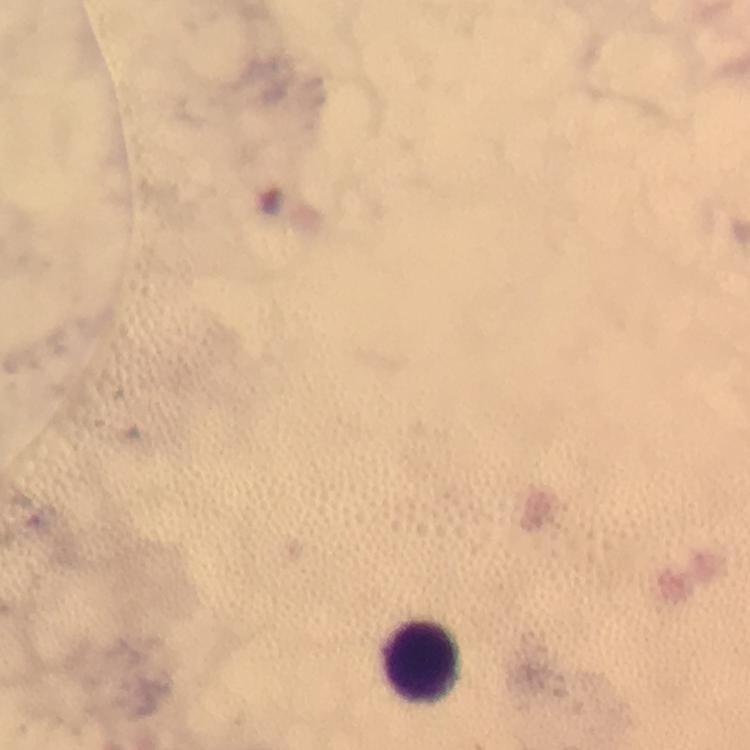
Approximate centers as (x, y) in pixels.
Summary:
  - Leukocyte locations: (427, 663)
  - Context: from a diagnostic examination for malaria
  - Capture: smartphone mounted on the microscope
  - Plasmodium parasites: none seen
  - Stain: Giemsa
  - Preparation: thick blood film
  - Image size: 750×750 pixels
  - Magnification: 100x
  - Immersion oil: applied
  - Cropped from: one field of view